Locate every blood parasite and identify its species.
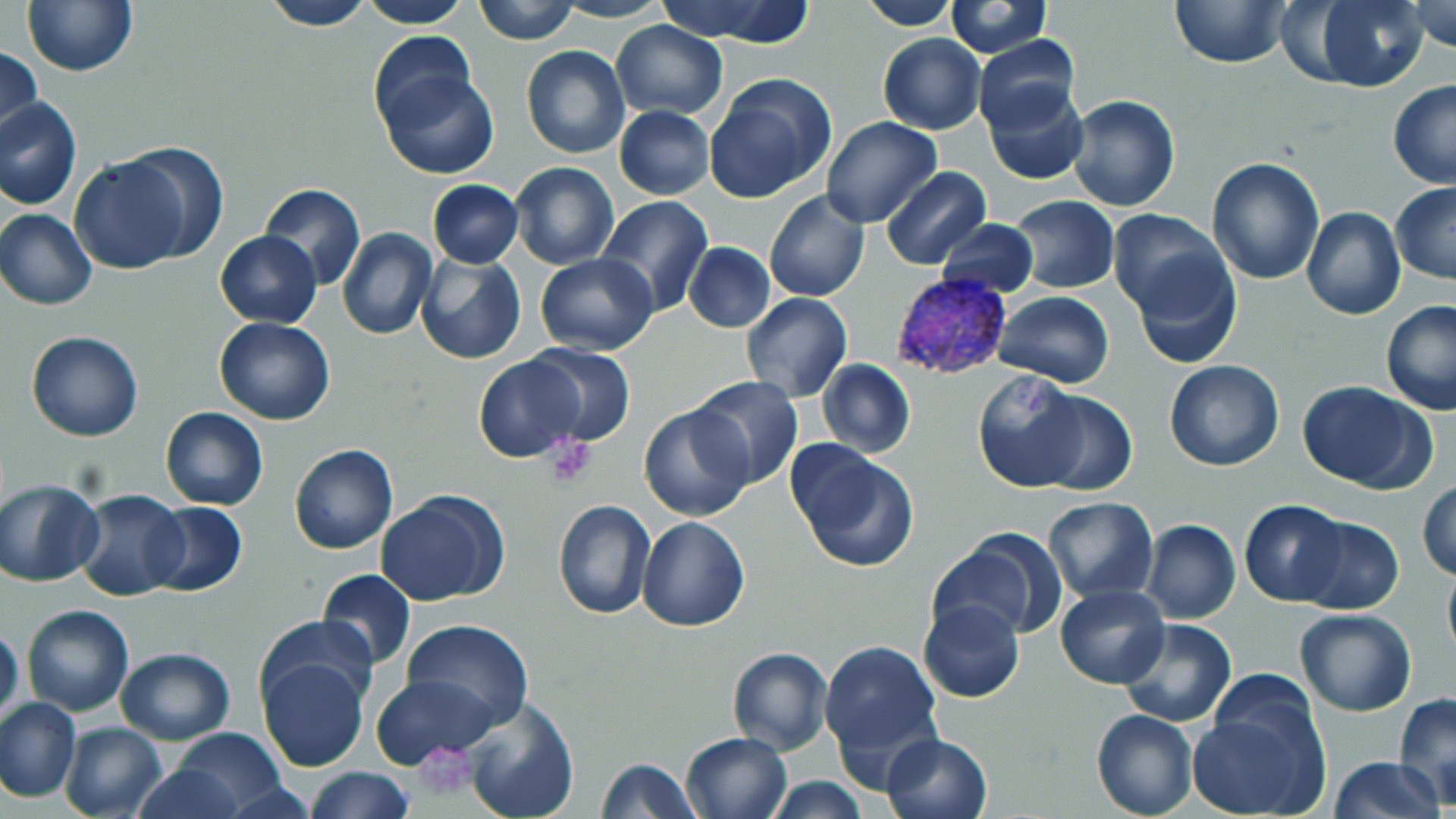

Approximate bounding boxes as [x1, y1, x2, y2] in pixels.
Plasmodium vivax-infected red blood cells: [888, 273, 1016, 384].
No Plasmodium falciparum, Plasmodium ovale, Plasmodium malariae, Babesia divergens, or Trypanosoma brucei observed.

Summary:
  - Uninfected red blood cell locations: [258, 0, 377, 30], [358, 0, 474, 27], [474, 0, 579, 44], [655, 0, 820, 45], [858, 0, 962, 29], [1169, 0, 1292, 70], [1303, 0, 1430, 91], [1406, 0, 1456, 51], [22, 1, 138, 76], [550, 1, 672, 23], [946, 1, 1052, 57], [610, 21, 728, 119], [877, 32, 985, 134], [367, 33, 479, 135], [974, 34, 1081, 134], [1, 46, 43, 146], [521, 46, 631, 160], [378, 66, 498, 180], [704, 74, 837, 202], [1387, 78, 1456, 190], [983, 84, 1089, 186], [1065, 95, 1180, 213], [0, 97, 81, 210], [614, 105, 714, 199], [821, 117, 942, 229], [113, 143, 228, 262], [67, 155, 194, 273], [1206, 156, 1326, 285], [509, 161, 620, 270], [883, 167, 990, 268], [427, 179, 522, 267], [1390, 182, 1456, 285], [259, 183, 365, 292], [764, 191, 871, 303], [594, 195, 715, 318], [1010, 196, 1118, 293], [1301, 207, 1406, 321], [1, 209, 96, 309], [1108, 211, 1228, 323], [935, 218, 1040, 298], [337, 228, 437, 342], [215, 231, 321, 327], [684, 242, 775, 332], [1126, 248, 1242, 368], [535, 253, 657, 355], [416, 254, 524, 365], [992, 291, 1115, 387], [740, 292, 852, 403], [1380, 300, 1456, 416], [213, 317, 335, 426], [25, 331, 143, 441], [523, 346, 636, 446], [475, 355, 589, 463], [816, 359, 914, 459], [1164, 359, 1284, 471], [972, 370, 1090, 491], [690, 377, 803, 490], [1296, 380, 1437, 493], [1029, 388, 1138, 496], [640, 404, 754, 521], [160, 407, 268, 510], [289, 443, 398, 555], [791, 447, 918, 573], [0, 479, 103, 587], [1418, 479, 1456, 581], [74, 489, 188, 602], [378, 491, 509, 607], [1043, 496, 1159, 601], [552, 499, 655, 621], [142, 501, 247, 595], [1239, 501, 1348, 606], [636, 516, 750, 632], [1292, 516, 1404, 615], [1140, 519, 1241, 624], [937, 527, 1064, 641], [1441, 561, 1456, 662], [317, 568, 416, 669], [1055, 585, 1170, 689], [918, 599, 1025, 703], [22, 604, 134, 716], [1295, 608, 1418, 715], [258, 614, 378, 718], [1118, 617, 1237, 727], [399, 618, 535, 730], [0, 624, 24, 730], [820, 638, 944, 759], [726, 646, 832, 757], [114, 647, 235, 744], [256, 651, 370, 773], [1212, 668, 1321, 766], [369, 670, 498, 767], [1393, 692, 1456, 804], [1188, 695, 1329, 819], [0, 697, 80, 802], [461, 698, 580, 819], [1090, 710, 1198, 819], [60, 721, 167, 819], [171, 729, 288, 814], [681, 731, 793, 819], [881, 732, 993, 819], [1327, 756, 1447, 819], [594, 758, 701, 819], [133, 762, 251, 819], [306, 765, 413, 819], [764, 777, 870, 817]
  - Platelet locations: [542, 436, 598, 488], [414, 741, 476, 798]
  - Slide-level diagnosis: Plasmodium vivax
  - Image size: 1456×819 pixels
  - Preparation: thin blood film
  - Magnification: 1000x
  - Stain: May-Grünwald-Giemsa
  - Modality: light microscopy
  - Field of view: single